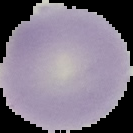 Malaria status: uninfected. Image is 133×133 pixels. The area outside the segmented cell region is set to black. From a thin blood smear.